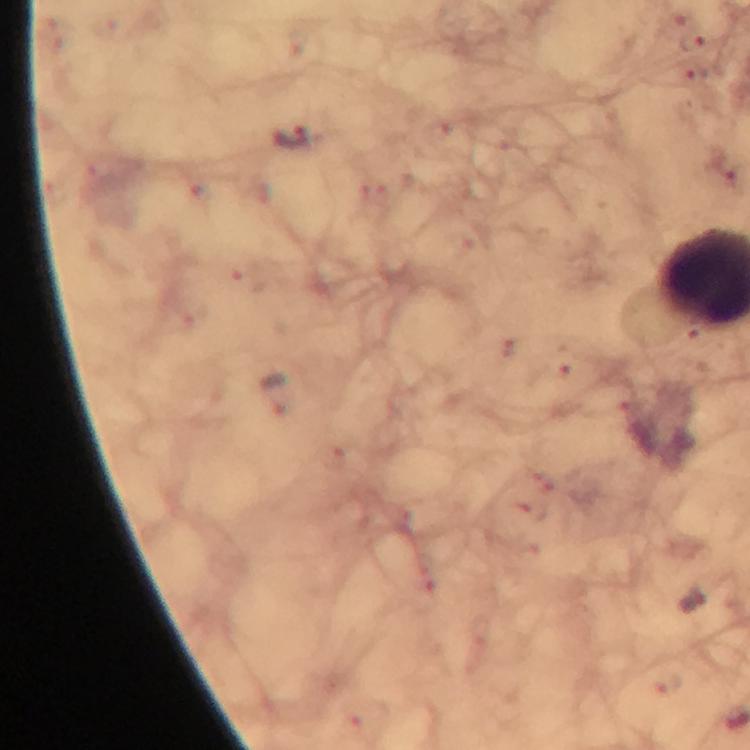
Approximate centers as [x, y] in pixels.
Summary:
  - Malaria parasite locations: [693, 41], [289, 137], [724, 165]
  - Context: from a diagnostic examination for malaria
  - Immersion oil: used
  - Magnification: 100x
  - Image size: 750×750 pixels
  - Capture: smartphone camera through the microscope
  - Preparation: thick blood film
  - Cropped from: one field of view
  - Stain: Giemsa